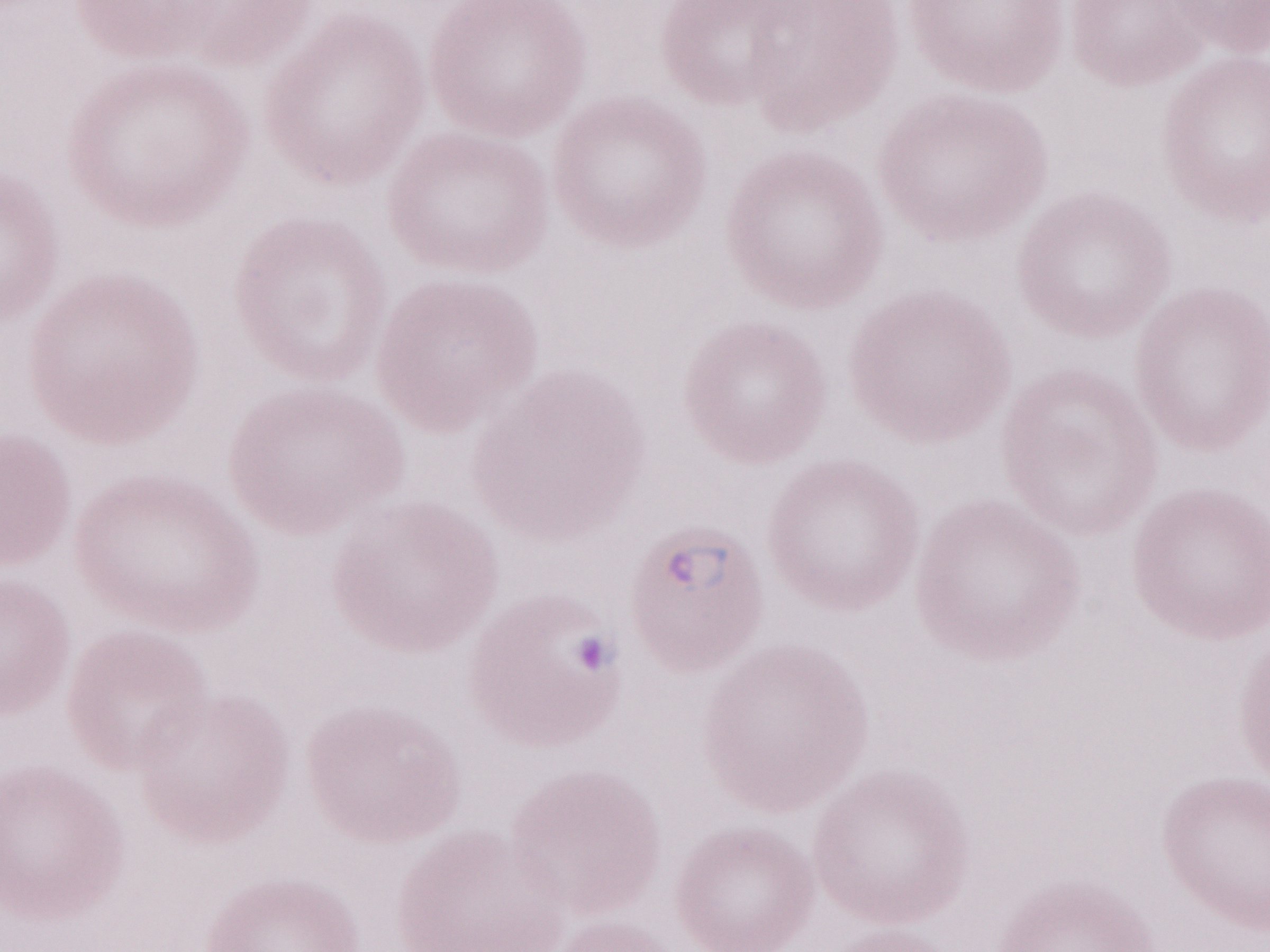
Patient-level malaria diagnosis: positive. Thin peripheral-blood smear. 1,000x magnification. Image is 1270×952 pixels. Olympus BX43 microscope, Olympus DP73 camera. May-Grünwald-Giemsa stain. Single field of view.